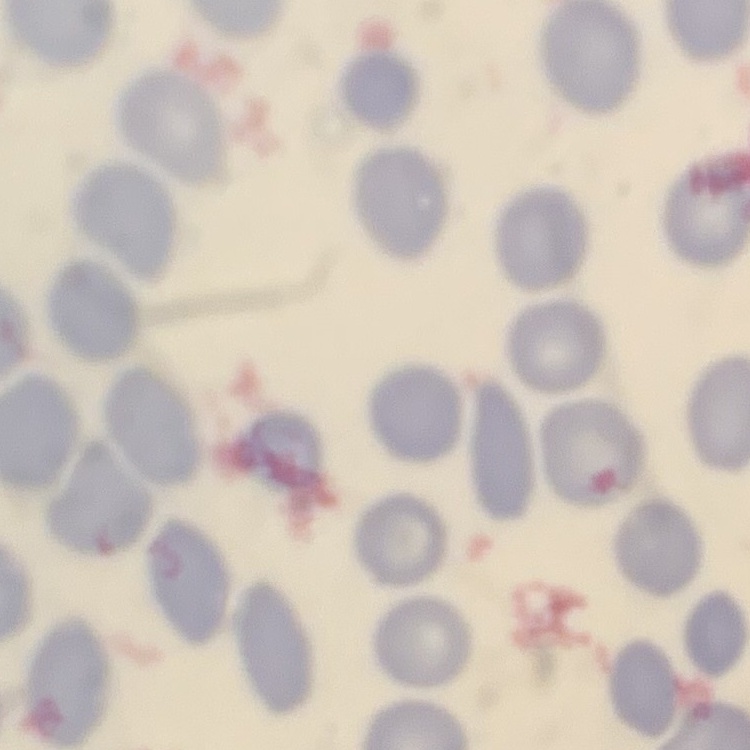 The erythrocytes exhibit no rouleaux formation. Thin blood film. Square crop of a larger photomicrograph. Field's or Giemsa stain.